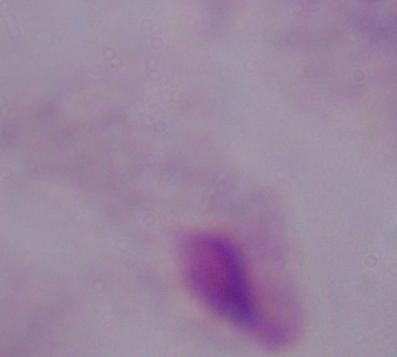

magnification: 1000x
modality: micrograph
identification: trichomonad